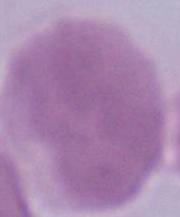 Photomicrograph. 1000x magnification. A red blood cell is seen.